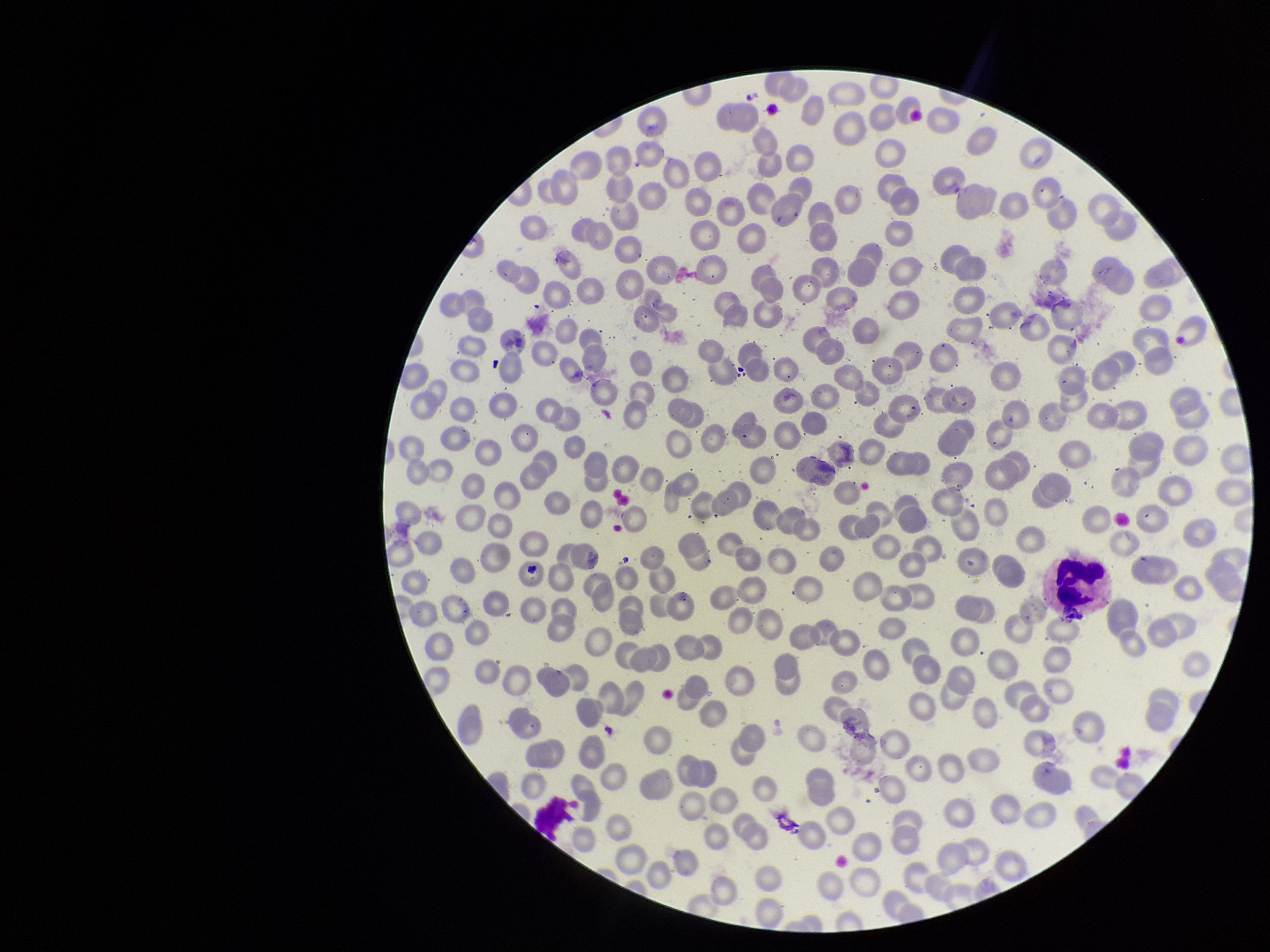
{
  "patient_malaria_status": "negative",
  "capture": "smartphone photograph through the microscope eyepiece",
  "red_blood_cell_count": 293,
  "preparation": "thin blood smear",
  "field_of_view": "single",
  "image_size": "1270×952 pixels",
  "stain": "Giemsa",
  "parasitized_red_blood_cell_count": 0,
  "parasitized_red_blood_cells": "none detected"
}